Report the malaria status of this cell.
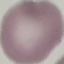

It is uninfected.

Summary:
  - Preparation: thin blood film
  - Image type: automatically extracted cell patch, resized to 64 × 64 pixels
  - Capture: smartphone through the microscope eyepiece
  - Stain: Giemsa